Assess this cell for malaria.
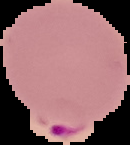
It is parasitized.

image_type: segmented cell region on a black background
image_size: 130×145 pixels
preparation: thin blood smear